Assess the morphology of the erythrocytes.
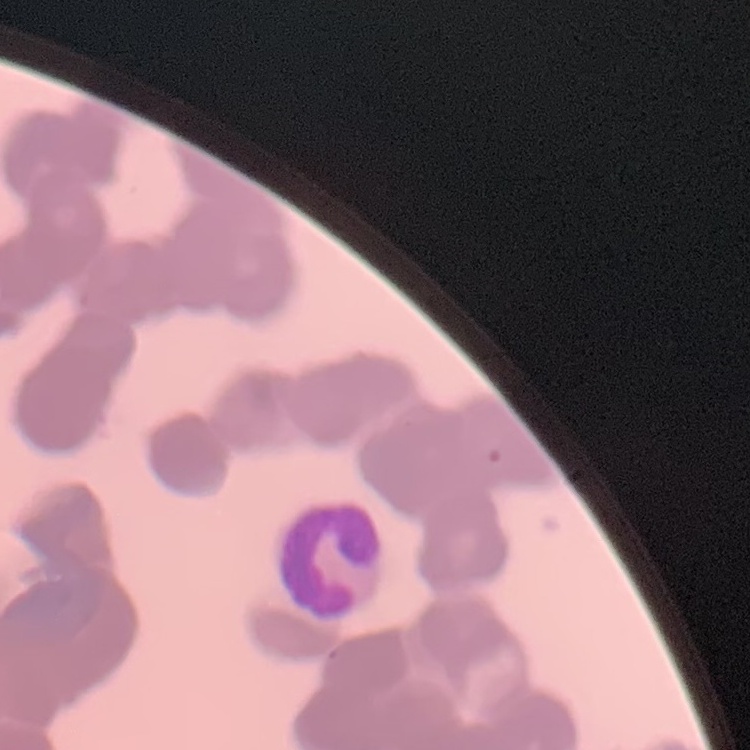

Rouleaux formation.

stain = Field's or Giemsa
image type = square crop of a larger photomicrograph
preparation = thin blood smear